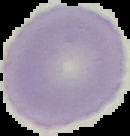

Summary:
  - Result: no Plasmodium parasites detected
  - Image size: 130×136 pixels
  - Image type: segmented cell region on a black background
  - Preparation: thin blood smear